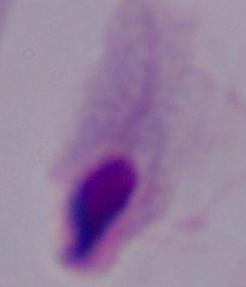
magnification: 1000x
identification: trichomonad
modality: photomicrograph